State which parasite is depicted.
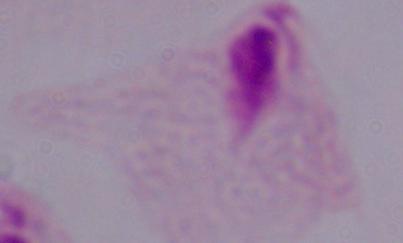
This is a trichomonad.

modality: micrograph
magnification: 1000x